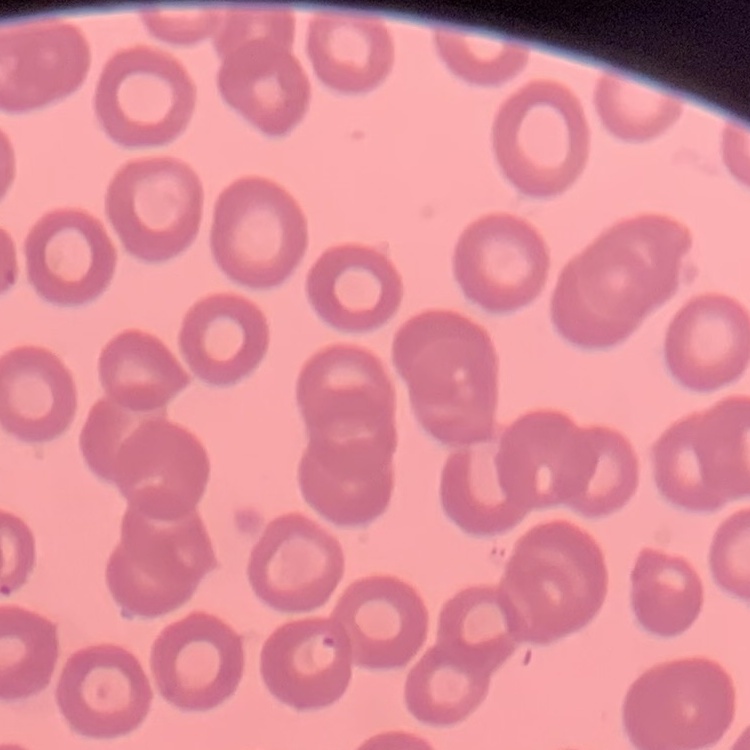
erythrocyte_morphology: no rouleaux formation
image_type: one tile cut from a larger photomicrograph
stain: Field's or Giemsa
preparation: thin blood film